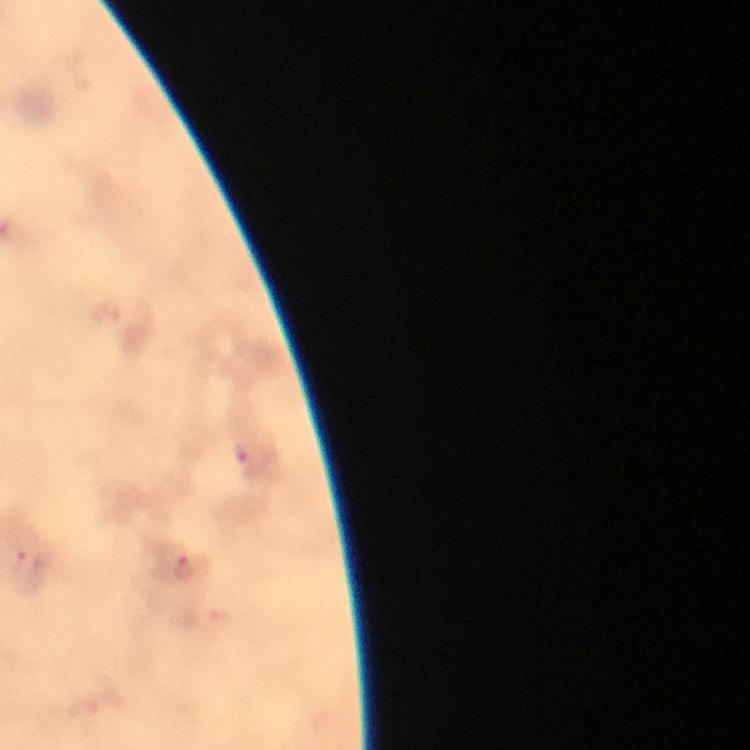
Approximate centers as (x, y) in pixels.
Summary:
  - Malaria parasite locations: (254, 459), (25, 565), (186, 567)
  - Image size: 750×750 pixels
  - Magnification: 100x
  - Immersion oil: used
  - Preparation: thick blood smear
  - Cropped from: a single field of view
  - Capture: smartphone photograph through a microscope
  - Stain: Giemsa
  - Context: from a malaria diagnostic workup